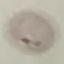

Summary:
  - Result: malaria parasites identified
  - Stain: Giemsa
  - Image type: automatically extracted cell patch, resized to 64 × 64 pixels
  - Capture: smartphone camera at the microscope eyepiece
  - Preparation: thin blood smear